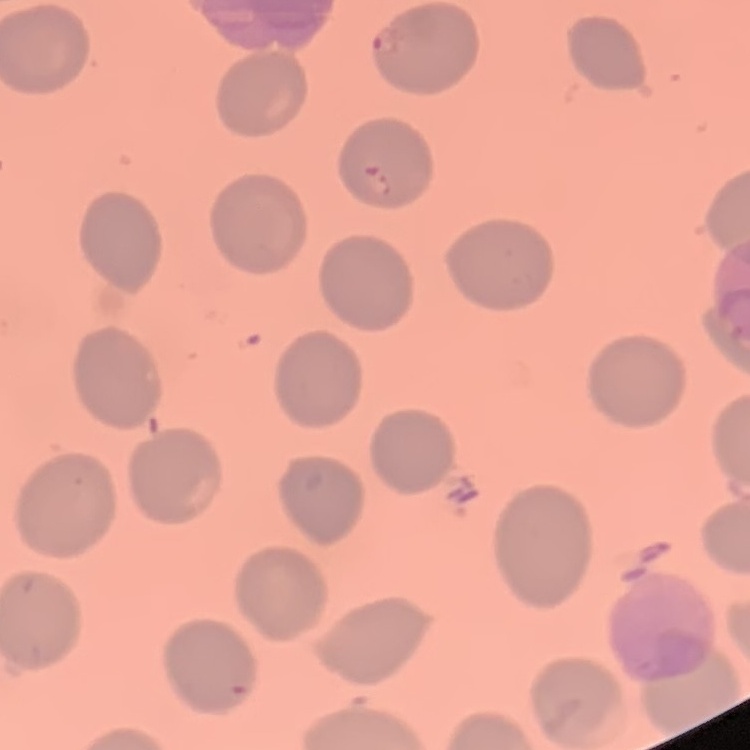
erythrocyte morphology = no rouleaux formation
image type = one tile cut from a larger photomicrograph
stain = Field's or Giemsa
preparation = thin peripheral smear